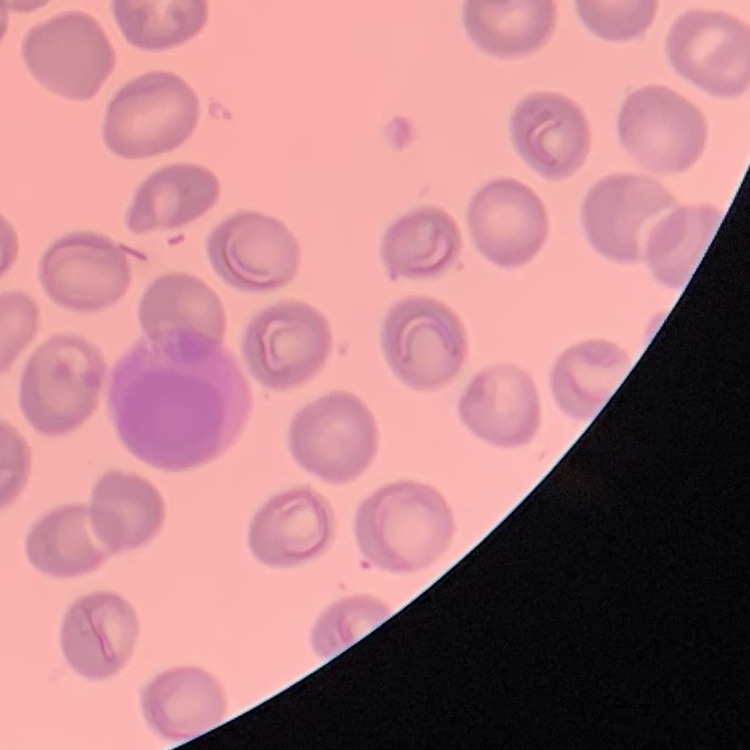
Summary:
  - Red blood cell morphology: no rouleaux formation
  - Stain: Field's or Giemsa
  - Image type: one tile cut from a larger photomicrograph
  - Preparation: thin blood film